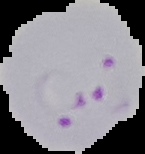

Summary:
  - Result: Plasmodium parasites detected
  - Preparation: thin blood film
  - Image type: segmented cell region on a black background
  - Image size: 145×154 pixels